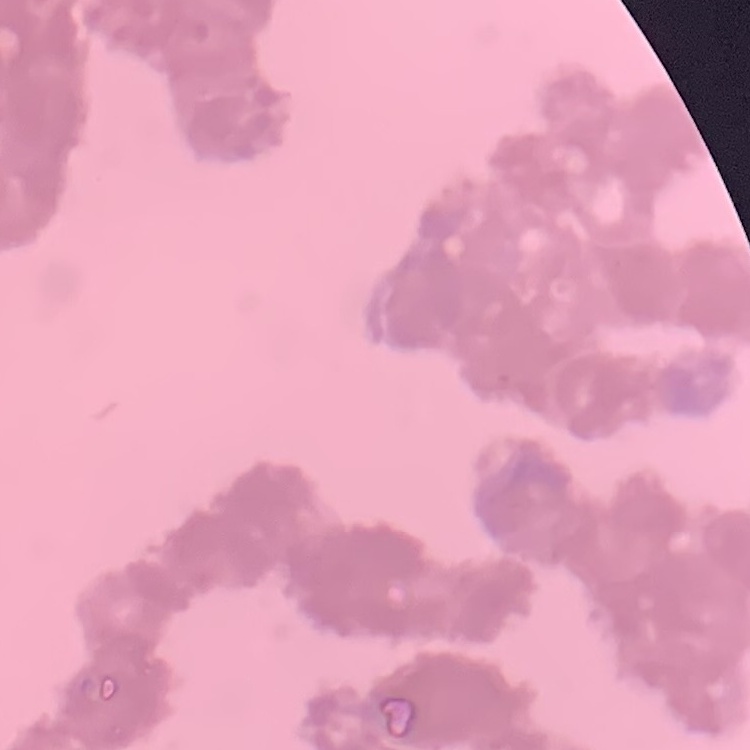

Summary:
  - Erythrocyte morphology: rouleaux formation
  - Image type: square crop of a larger photomicrograph
  - Preparation: thin peripheral smear
  - Stain: Field's or Giemsa